Locate every malaria parasite.
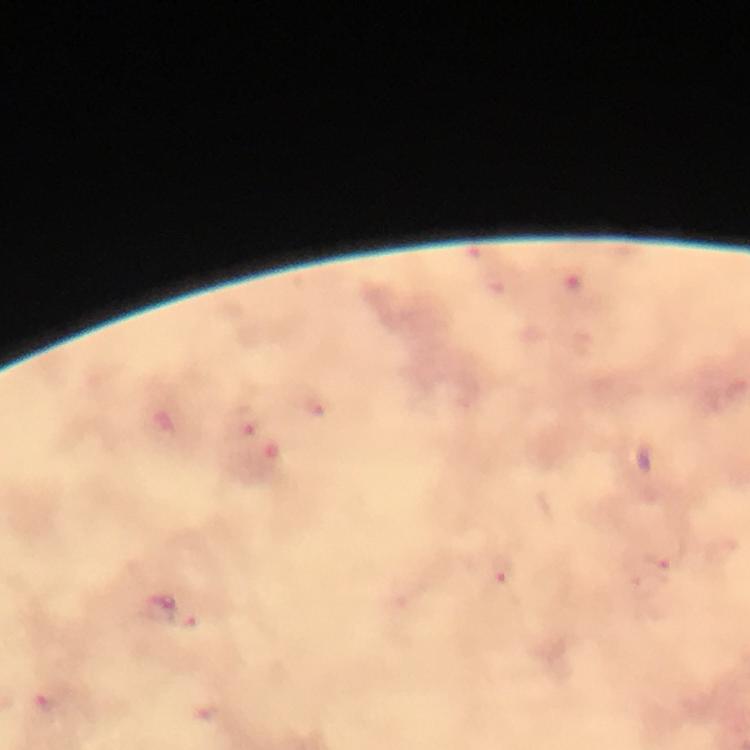

Approximate centers as {x, y} in pixels.
Malaria parasites: {248, 420}, {657, 567}, {502, 572}, {49, 705}.

magnification: 100x
cropped_from: a single field of view
preparation: thick blood smear
context: from a malaria diagnostic workup
image_size: 750×750 pixels
capture: smartphone photograph through a microscope
immersion_oil: used
stain: Giemsa